Comment on the morphology of the erythrocytes.
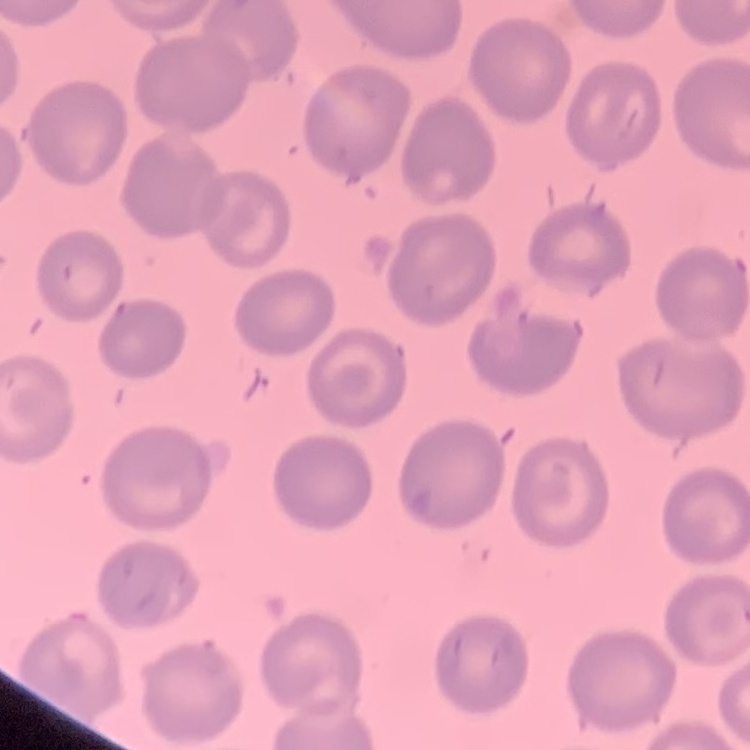

No rouleaux formation.

Field's or Giemsa stain. Square crop of a larger photomicrograph. Thin blood smear.